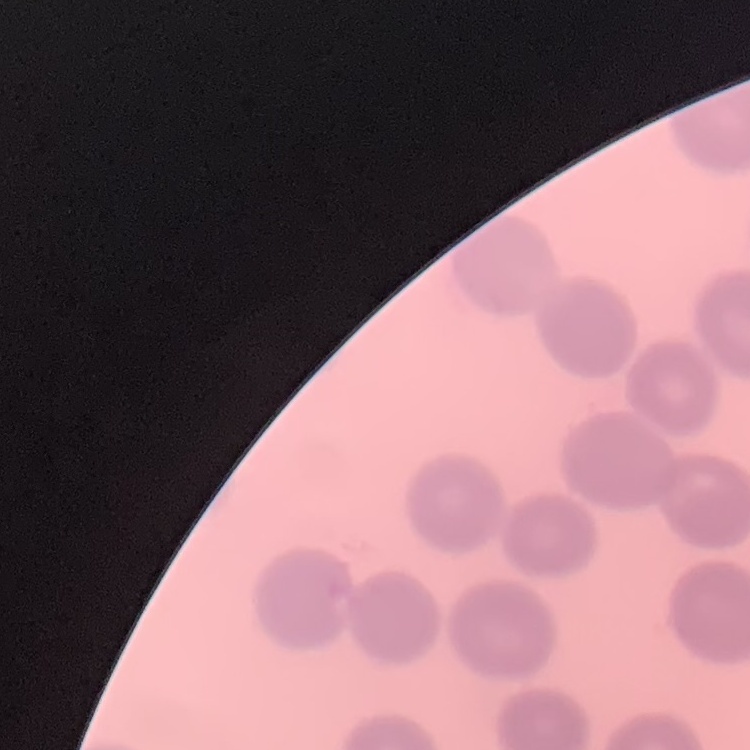
The erythrocytes show no rouleaux formation. Square crop of a larger photomicrograph. Thin blood smear. Stained with either Field's or Giemsa.